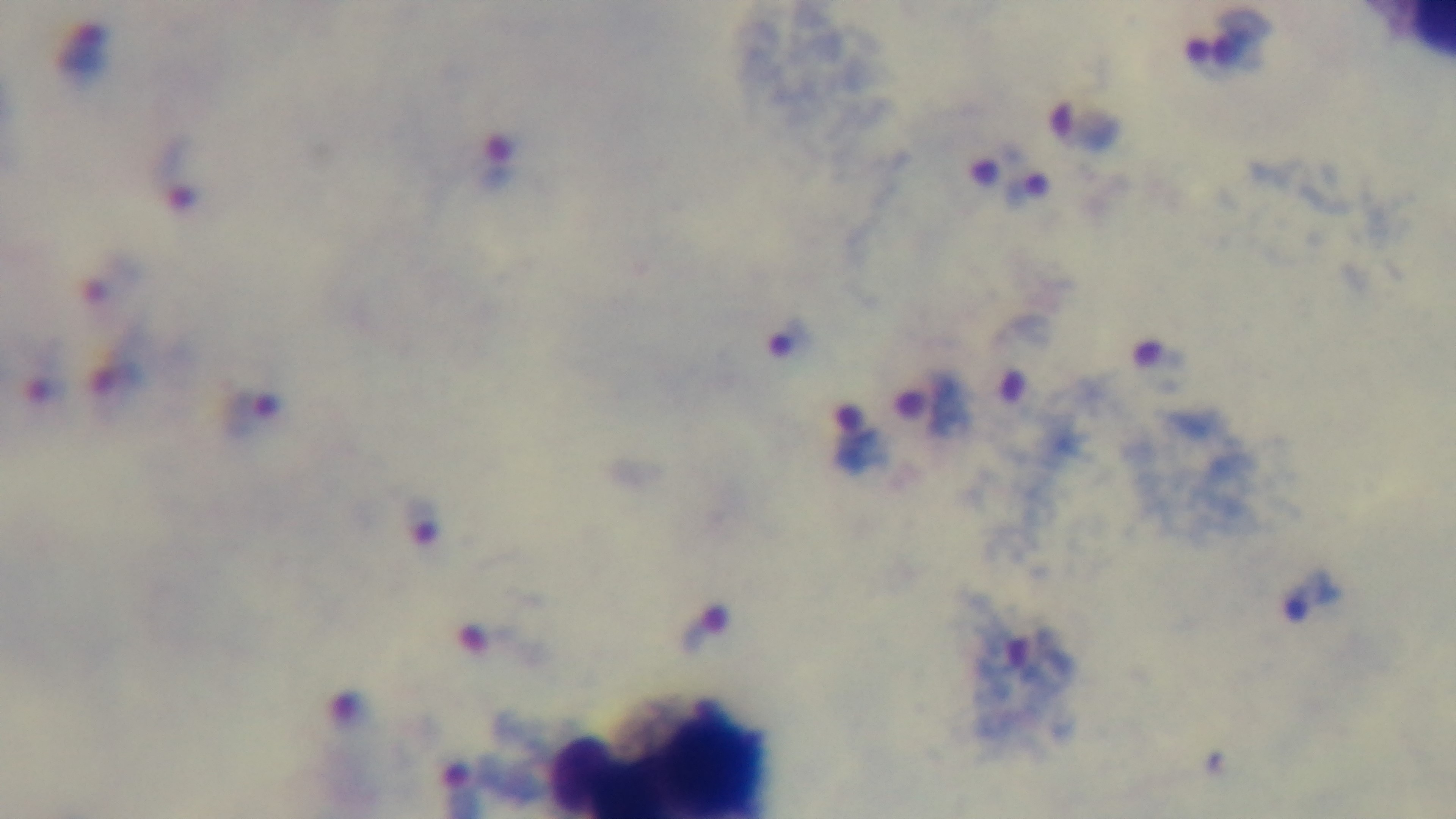
Summary:
  - Modality: light microscopy
  - Stain: Giemsa
  - Capture: mounted 4K digital camera
  - Malaria status: positive
  - Field of view: one from the slide
  - Objective: 100x oil immersion
  - Preparation: thick